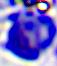

modality = micrograph
magnification = 400x
identification = white blood cell